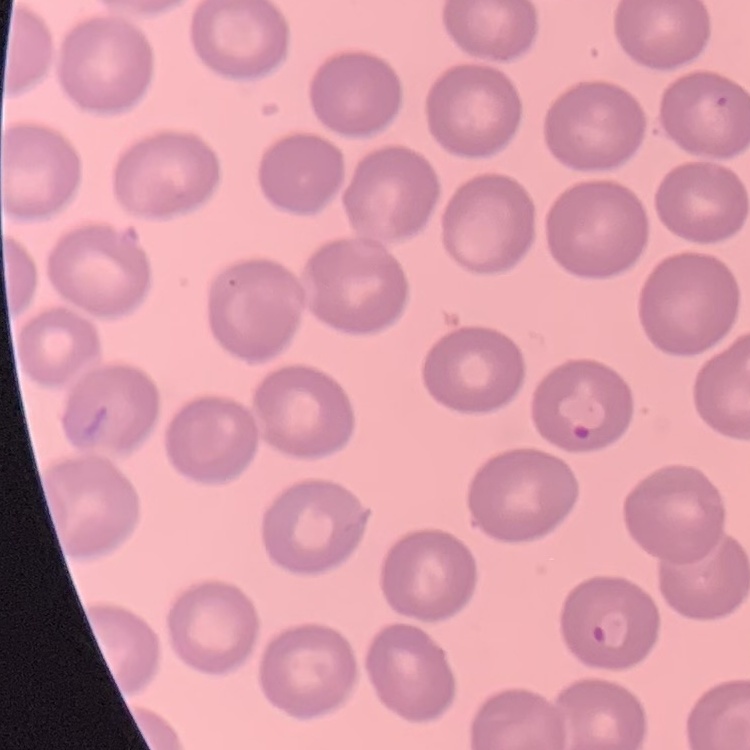
erythrocyte morphology = no rouleaux formation
image type = square crop of a larger photomicrograph
stain = Field's or Giemsa
preparation = thin peripheral smear